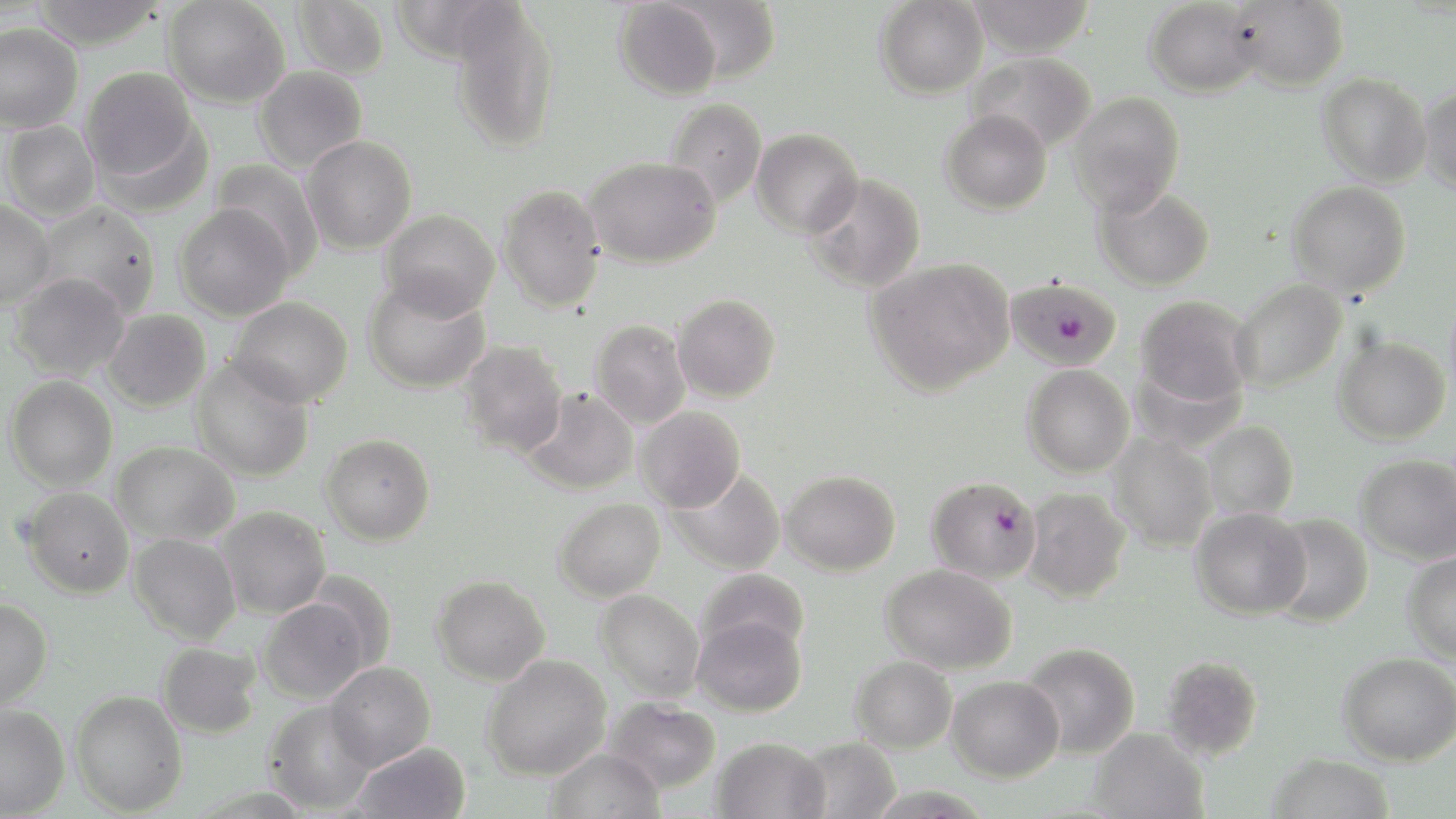

Summary:
  - Coordinate format: approximate bounding boxes as (x1,y1)-(x2,y2) corner pairs in pixels
  - Uninfected red blood cell locations: (31,0)-(167,50), (163,0)-(290,108), (291,0)-(390,79), (668,0)-(780,83), (874,0)-(988,99), (966,0)-(1096,57), (1144,0)-(1263,98), (614,1)-(723,101), (1228,1)-(1349,91), (450,2)-(560,153), (0,23)-(83,133), (966,52)-(1097,154), (253,65)-(368,174), (81,67)-(201,187), (1317,72)-(1432,187), (1419,83)-(1456,195), (1068,91)-(1185,217), (665,99)-(767,208), (940,108)-(1052,216), (1,120)-(100,222), (751,128)-(863,238), (301,135)-(417,253), (584,156)-(721,268), (211,160)-(325,276), (803,173)-(926,294), (1288,181)-(1411,296), (1094,184)-(1215,291), (498,185)-(605,313), (0,200)-(56,309), (35,202)-(161,318), (174,203)-(294,321), (380,209)-(499,320), (865,257)-(1015,396), (9,273)-(130,381), (364,275)-(491,393), (1230,279)-(1347,392), (673,294)-(781,402), (1135,296)-(1254,410), (229,297)-(353,407), (102,309)-(211,412), (591,320)-(691,429), (1333,335)-(1450,445), (457,341)-(568,457), (190,358)-(315,482), (1022,364)-(1135,478), (5,375)-(118,491), (520,388)-(638,495), (636,406)-(746,512), (1200,421)-(1298,521), (1107,432)-(1218,552), (320,433)-(435,545), (113,441)-(239,545), (1356,454)-(1456,563), (666,467)-(786,575), (781,470)-(901,576), (21,487)-(134,598), (1022,487)-(1131,603), (554,497)-(665,602), (215,506)-(331,618), (1191,507)-(1311,619), (1265,514)-(1374,627), (129,533)-(241,644), (1403,551)-(1456,663), (881,563)-(1018,675), (696,568)-(810,659), (431,575)-(551,686), (595,589)-(705,703), (0,596)-(53,709), (257,597)-(372,704), (692,615)-(807,717), (157,642)-(263,739), (1019,642)-(1140,759), (1338,652)-(1456,765), (482,653)-(612,781), (1160,655)-(1264,760), (851,656)-(957,754), (325,662)-(436,770), (947,676)-(1064,782), (70,689)-(187,815), (605,697)-(721,794), (264,700)-(377,815), (0,704)-(70,818), (1088,727)-(1209,819), (712,737)-(830,819), (794,737)-(901,819), (349,741)-(471,819), (547,747)-(664,819), (1267,752)-(1394,819)
  - Plasmodium falciparum-infected red blood cell locations: (1006,277)-(1121,371), (926,476)-(1041,583)
  - Slide-level diagnosis: Plasmodium falciparum
  - Image size: 1456×819 pixels
  - Field of view: single
  - Modality: optical microscopy
  - Stain: May-Grünwald-Giemsa
  - Magnification: 1000x
  - Preparation: thin blood film